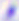
magnification = 400x
identification = Toxoplasma gondii
modality = photomicrograph